Give the extent of all Plasmodium falciparum-infected red blood cells.
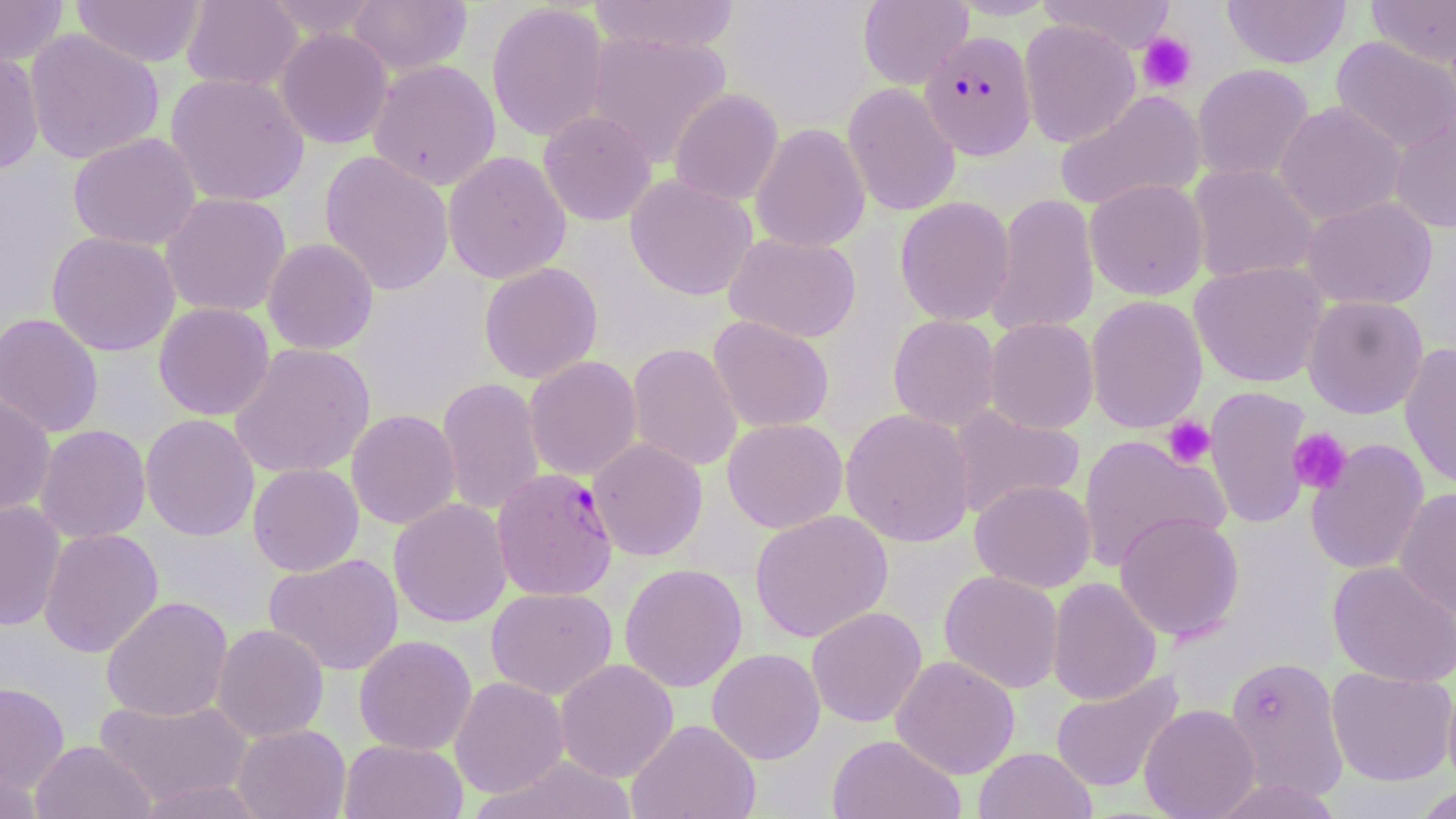
Approximate bounding boxes as (x1,y1)-(x2,y2) corner pairs in pixels.
Plasmodium falciparum-infected red blood cells: (919,30)-(1037,160), (492,468)-(617,601).

Summary:
  - Platelet locations: (1136,32)-(1197,94), (1163,415)-(1215,469), (1287,427)-(1353,494)
  - Uninfected red blood cell locations: (0,0)-(68,67), (71,0)-(207,68), (181,0)-(303,92), (263,0)-(383,39), (348,0)-(472,76), (588,0)-(741,55), (857,0)-(972,89), (1039,0)-(1177,54), (1222,0)-(1352,69), (1365,0)-(1456,68), (486,2)-(610,142), (1019,19)-(1140,148), (275,27)-(394,149), (24,28)-(165,164), (586,30)-(732,168), (1331,36)-(1456,154), (0,49)-(45,176), (367,59)-(501,190), (1192,64)-(1314,182), (165,72)-(309,207), (842,83)-(961,217), (669,89)-(783,205), (1054,90)-(1207,212), (1274,101)-(1407,225), (537,110)-(657,226), (1389,110)-(1456,233), (750,122)-(870,253), (68,132)-(202,251), (319,150)-(454,296), (443,151)-(571,284), (1187,164)-(1319,284), (625,175)-(757,301), (1084,179)-(1209,301), (160,192)-(291,317), (987,192)-(1100,337), (895,196)-(1015,326), (1301,196)-(1438,310), (46,230)-(180,356), (723,232)-(862,343), (263,238)-(378,355), (1190,261)-(1328,388), (479,262)-(603,383), (1085,295)-(1208,433), (1303,295)-(1428,419), (153,302)-(275,420), (0,312)-(104,438), (888,314)-(1001,431), (708,315)-(834,433), (984,318)-(1099,434), (230,342)-(376,479), (627,342)-(743,472), (1400,343)-(1456,490), (524,356)-(642,480), (437,376)-(545,516), (1203,386)-(1313,529), (0,394)-(56,519), (947,404)-(1086,520), (840,408)-(976,547), (346,409)-(461,530), (140,413)-(260,541), (722,418)-(848,533), (34,425)-(151,544), (1077,434)-(1229,572), (587,437)-(708,561), (1306,439)-(1429,575), (248,463)-(364,576), (970,479)-(1096,592), (1394,487)-(1456,621), (389,498)-(512,627), (0,501)-(66,631), (750,509)-(893,643), (1114,512)-(1245,642), (39,528)-(163,658), (263,552)-(404,675), (1328,560)-(1456,687), (620,563)-(747,692), (939,570)-(1064,693), (1047,577)-(1162,706), (486,587)-(617,699), (101,595)-(233,722), (806,606)-(927,728), (211,624)-(329,743), (353,634)-(476,755), (707,647)-(825,764), (1224,654)-(1348,803), (891,655)-(1020,779), (555,658)-(678,782), (1326,666)-(1456,786), (1050,671)-(1183,793), (450,676)-(570,798), (1442,676)-(1456,796), (0,682)-(70,793), (94,695)-(254,808), (1139,704)-(1260,819), (626,718)-(761,819), (232,724)-(351,819), (826,734)-(965,819), (339,739)-(468,819), (31,740)-(155,819), (973,747)-(1097,819), (476,755)-(638,819), (1,766)-(43,818), (1209,778)-(1344,819), (133,779)-(269,818), (1411,784)-(1456,819)
  - Slide-level diagnosis: Plasmodium falciparum
  - Preparation: thin blood film
  - Stain: May-Grünwald-Giemsa
  - Modality: light microscopy
  - Image size: 1456×819 pixels
  - Field of view: single
  - Magnification: 1000x